State which parasite is depicted.
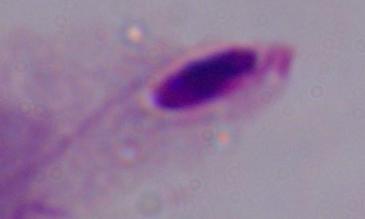
A trichomonad.

{
  "magnification": "1000x",
  "modality": "micrograph"
}